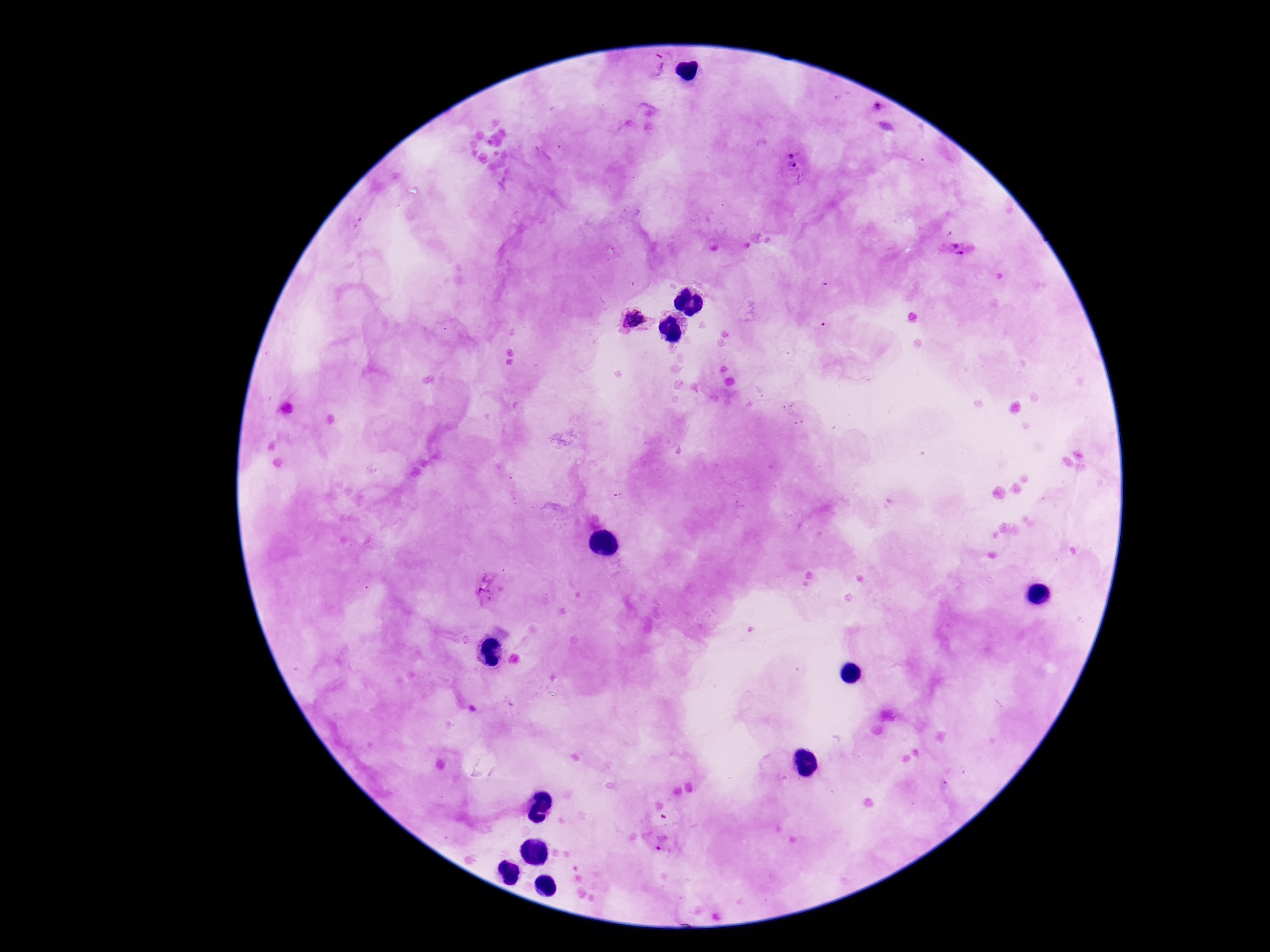
field of view = one from this slide
stain = Giemsa
patient malaria status = infected
capture = smartphone camera through the microscope eyepiece
magnification = 100x
image size = 1270×952 pixels
preparation = thick blood film
Plasmodium parasite locations = approximate centers as (x, y) in pixels: (656, 65), (877, 108), (793, 162), (956, 248), (637, 320), (491, 589), (663, 841)